Locate the Plasmodium falciparum-infected red blood cells and any of indeterminate infection status.
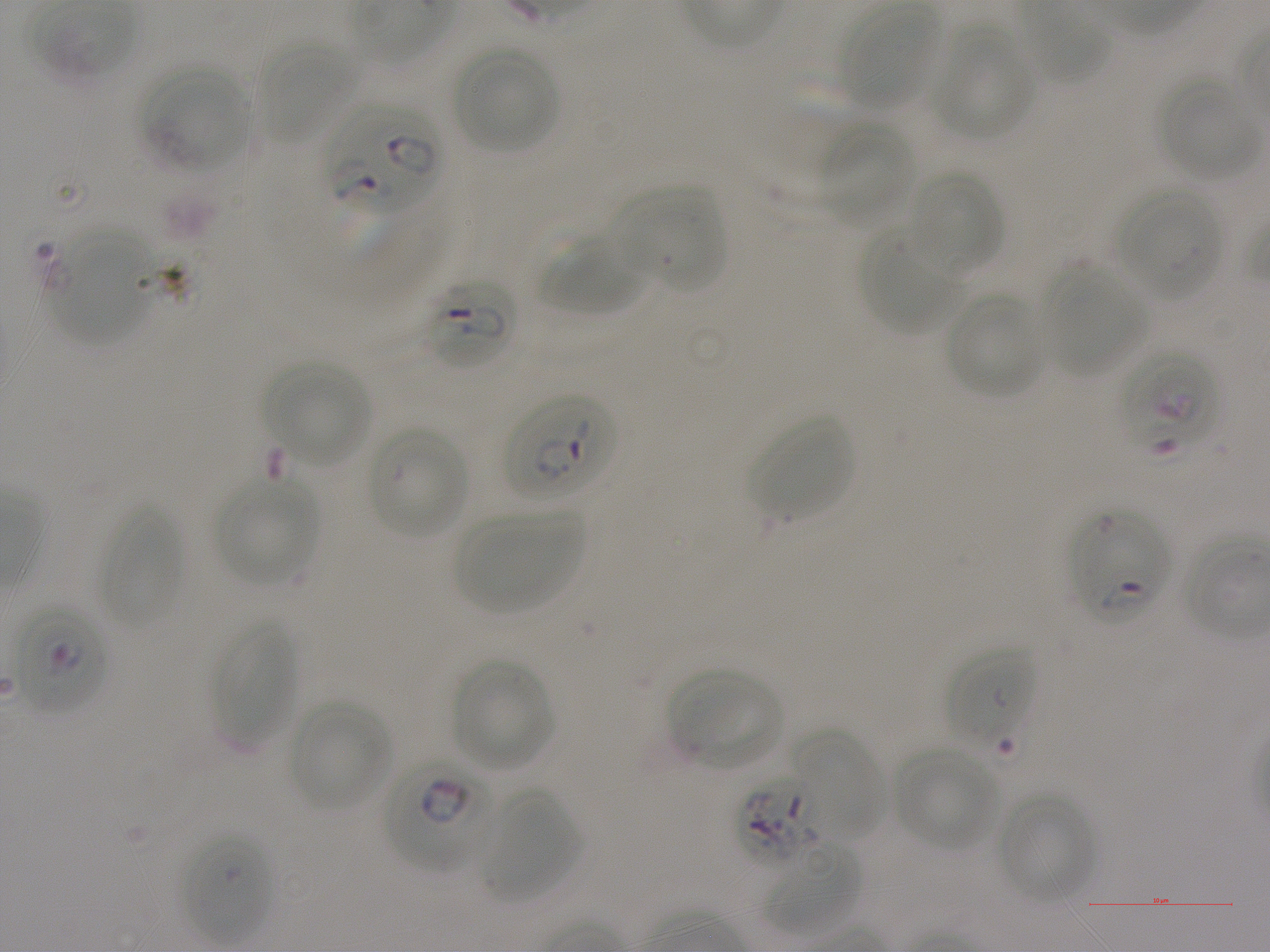
Approximate bounding boxes as {x1, y1, x2, y2} in pixels. Not every red blood cell is marked. A life-cycle stage — or a range of stages, where the recorded stages span more than one — follows each staged infected red blood cell.
Infected red blood cells: {324, 103, 442, 214}; {421, 276, 517, 370} early ring to early trophozoite; {504, 394, 616, 503} early ring to early trophozoite; {1070, 508, 1170, 623} ring; {12, 603, 108, 715} late ring to early trophozoite; {385, 754, 497, 873} late ring to early trophozoite; {737, 775, 826, 866}.
Red blood cells of indeterminate infection status: {1119, 347, 1221, 459}, {947, 645, 1035, 752}, {181, 829, 271, 943}.

Summary:
  - Locations of uninfected red blood cells: {838, 5, 939, 110}, {1014, 7, 1111, 86}, {931, 27, 1033, 140}, {257, 42, 357, 144}, {452, 45, 560, 154}, {141, 64, 251, 170}, {1157, 75, 1259, 180}, {817, 121, 912, 227}, {906, 170, 1004, 278}, {612, 186, 726, 293}, {1115, 186, 1222, 300}, {48, 227, 153, 344}, {859, 227, 962, 334}, {544, 236, 646, 317}, {1041, 264, 1147, 376}, {943, 291, 1047, 399}, {265, 361, 370, 466}, {749, 416, 855, 522}, {367, 424, 469, 539}, {214, 477, 318, 586}, {98, 501, 181, 632}, {454, 510, 582, 614}, {212, 618, 297, 751}, {450, 658, 556, 772}, {669, 671, 783, 770}, {289, 702, 390, 810}, {793, 730, 884, 842}, {893, 748, 997, 849}, {479, 788, 578, 903}, {997, 792, 1094, 905}, {764, 841, 861, 937}
  - Culture: Plasmodium falciparum strain NF54, static, in vitro
  - Stain: Giemsa
  - Donor blood group: A+
  - Field of view: one from this slide
  - Image size: 1270×952 pixels
  - Preparation: thin blood smear
  - Objective: 100x, oil immersion, numerical aperture 1.25